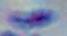 Toxoplasma gondii is shown. Photomicrograph. 1000x magnification.